State the blood parasite species.
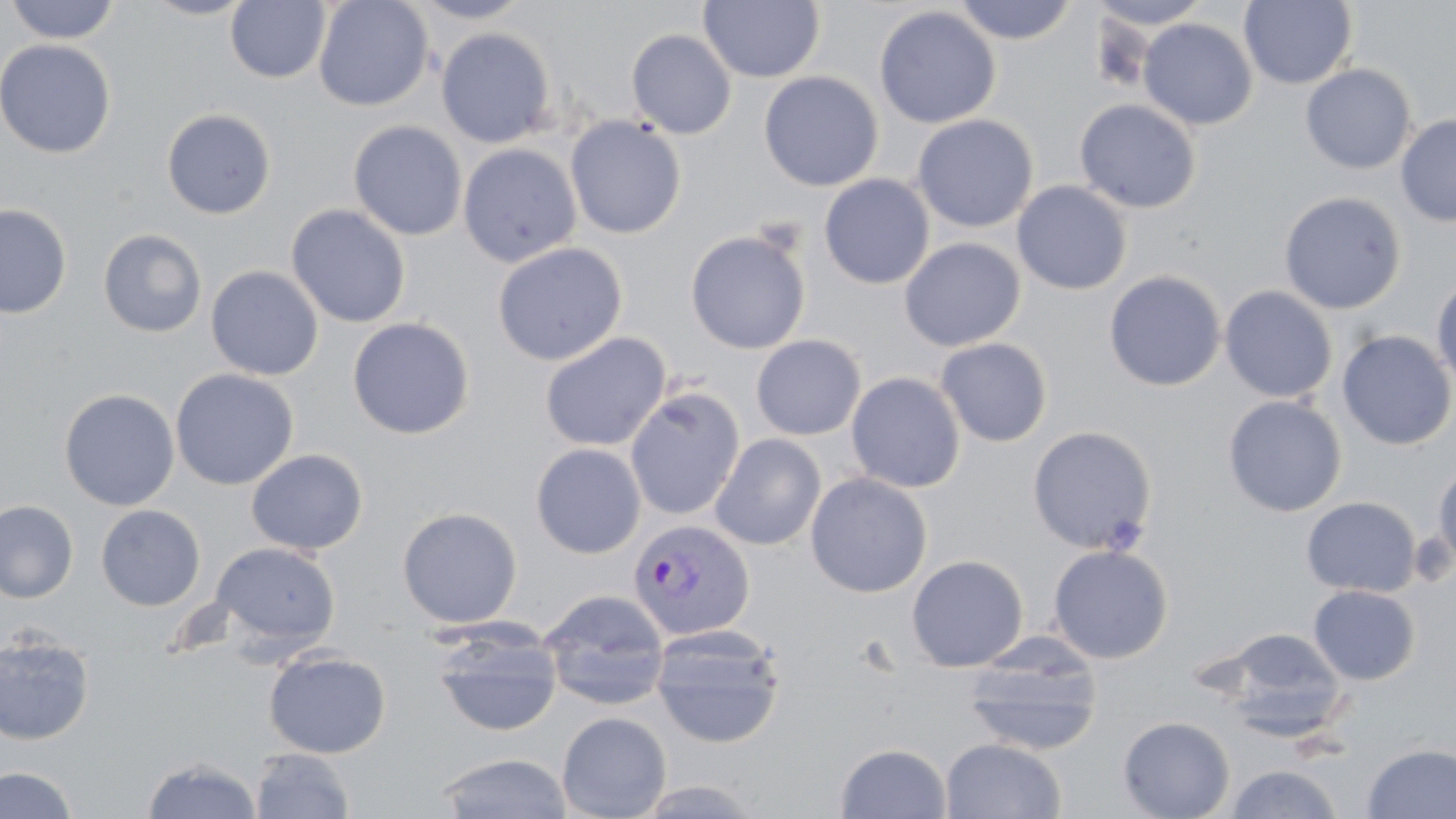

Plasmodium vivax.

Summary:
  - Coordinate format: approximate bounding boxes as named x1/y1/x2/y2 corners in pixels
  - Uninfected red blood cell locations: (x1=143, y1=0, x2=257, y2=20), (x1=313, y1=0, x2=434, y2=111), (x1=410, y1=0, x2=533, y2=24), (x1=698, y1=0, x2=825, y2=83), (x1=951, y1=0, x2=1078, y2=44), (x1=1086, y1=0, x2=1215, y2=29), (x1=4, y1=1, x2=121, y2=45), (x1=225, y1=1, x2=331, y2=83), (x1=1239, y1=1, x2=1358, y2=89), (x1=874, y1=5, x2=1002, y2=129), (x1=1138, y1=18, x2=1258, y2=130), (x1=436, y1=27, x2=557, y2=148), (x1=626, y1=28, x2=737, y2=139), (x1=0, y1=39, x2=117, y2=159), (x1=1300, y1=63, x2=1417, y2=174), (x1=758, y1=70, x2=884, y2=191), (x1=1074, y1=98, x2=1201, y2=214), (x1=161, y1=108, x2=276, y2=219), (x1=564, y1=114, x2=687, y2=240), (x1=912, y1=114, x2=1039, y2=233), (x1=1396, y1=114, x2=1456, y2=227), (x1=347, y1=120, x2=468, y2=241), (x1=458, y1=143, x2=582, y2=267), (x1=818, y1=174, x2=935, y2=290), (x1=1011, y1=180, x2=1132, y2=295), (x1=1279, y1=190, x2=1407, y2=314), (x1=0, y1=203, x2=72, y2=319), (x1=286, y1=203, x2=410, y2=328), (x1=97, y1=228, x2=208, y2=338), (x1=685, y1=229, x2=811, y2=354), (x1=899, y1=237, x2=1026, y2=352), (x1=492, y1=241, x2=628, y2=366), (x1=205, y1=265, x2=324, y2=381), (x1=1103, y1=270, x2=1226, y2=391), (x1=1431, y1=271, x2=1456, y2=393), (x1=1220, y1=285, x2=1338, y2=403), (x1=347, y1=317, x2=475, y2=440), (x1=1337, y1=330, x2=1456, y2=450), (x1=539, y1=332, x2=671, y2=452), (x1=751, y1=334, x2=866, y2=440), (x1=934, y1=337, x2=1053, y2=447), (x1=170, y1=368, x2=299, y2=490), (x1=846, y1=371, x2=966, y2=493), (x1=625, y1=386, x2=745, y2=522), (x1=59, y1=388, x2=180, y2=511), (x1=1222, y1=395, x2=1347, y2=517), (x1=1026, y1=425, x2=1158, y2=555), (x1=710, y1=433, x2=827, y2=550), (x1=530, y1=443, x2=646, y2=559), (x1=246, y1=448, x2=368, y2=555), (x1=1431, y1=461, x2=1456, y2=575), (x1=805, y1=472, x2=933, y2=598), (x1=1301, y1=496, x2=1421, y2=598), (x1=0, y1=499, x2=79, y2=603), (x1=95, y1=504, x2=206, y2=611), (x1=397, y1=506, x2=523, y2=628), (x1=210, y1=541, x2=341, y2=654), (x1=1047, y1=544, x2=1174, y2=664), (x1=906, y1=554, x2=1029, y2=672), (x1=1307, y1=585, x2=1420, y2=686), (x1=538, y1=588, x2=670, y2=711), (x1=429, y1=621, x2=564, y2=737), (x1=650, y1=625, x2=786, y2=748), (x1=1218, y1=627, x2=1348, y2=736), (x1=0, y1=631, x2=95, y2=745), (x1=961, y1=636, x2=1104, y2=756), (x1=264, y1=648, x2=391, y2=759), (x1=557, y1=711, x2=671, y2=819), (x1=1118, y1=715, x2=1235, y2=819), (x1=940, y1=737, x2=1067, y2=819), (x1=1361, y1=742, x2=1456, y2=818), (x1=835, y1=743, x2=952, y2=818), (x1=250, y1=747, x2=355, y2=819), (x1=436, y1=752, x2=573, y2=818), (x1=141, y1=755, x2=263, y2=818), (x1=1224, y1=764, x2=1344, y2=819), (x1=0, y1=765, x2=79, y2=817)
  - Plasmodium vivax-infected red blood cell locations: (x1=628, y1=518, x2=756, y2=641)
  - Magnification: 1000x
  - Field of view: one of a larger specimen
  - Image size: 1456×819 pixels
  - Modality: optical microscopy
  - Stain: May-Grünwald-Giemsa
  - Preparation: thin blood smear